State which parasite is depicted.
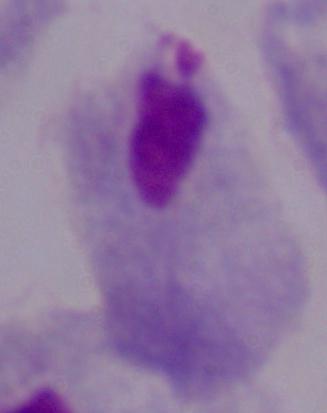
A trichomonad.

1000x magnification. Micrograph.